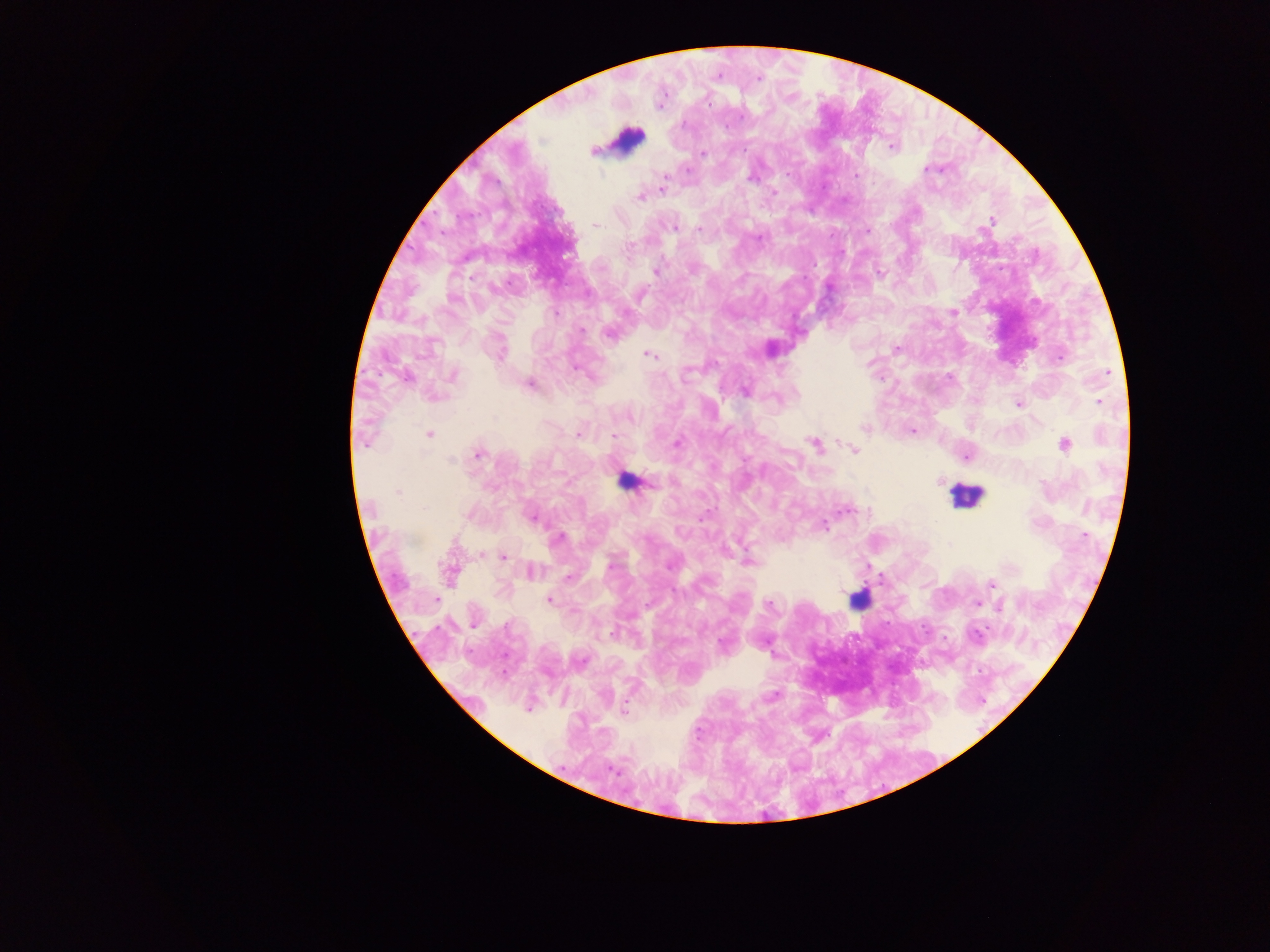
{
  "image_size": "1270×952 pixels",
  "capture": "mobile-phone photograph through a microscope",
  "leukocyte_locations": "approximate centers as {x, y} in pixels: {626, 139}, {626, 482}, {965, 495}, {858, 599}",
  "preparation": "thick blood film",
  "country": "Ghana",
  "malaria_parasite_locations": "approximate centers as {x, y} in pixels: {717, 77}, {759, 78}, {709, 104}, {742, 116}, {891, 147}, {593, 152}, {703, 154}, {687, 169}, {927, 169}, {855, 175}, {664, 178}, {750, 178}, {663, 189}, {774, 192}, {640, 198}, {990, 221}, {595, 224}, {675, 228}, {699, 229}, {867, 231}, {759, 238}, {629, 246}, {655, 271}, {953, 312}, {556, 314}, {582, 330}, {608, 334}, {897, 349}, {501, 354}, {648, 355}, {1060, 357}, {576, 369}, {1107, 373}, {453, 375}, {406, 377}, {685, 378}, {530, 384}, {745, 391}, {1099, 402}, {1018, 404}, {630, 419}, {865, 428}, {913, 431}, {429, 435}, {578, 435}, {614, 435}, {677, 443}, {815, 445}, {1065, 445}, {853, 450}, {479, 454}, {966, 456}, {451, 460}, {940, 481}, {398, 492}, {424, 508}, {847, 510}, {468, 514}, {532, 517}, {824, 525}, {1085, 535}, {559, 538}, {949, 543}, {481, 554}, {504, 557}, {749, 561}, {610, 566}, {531, 570}, {449, 573}, {569, 577}, {991, 584}, {550, 600}, {977, 603}, {769, 605}, {999, 606}, {475, 623}, {613, 633}, {975, 635}, {773, 697}, {625, 709}, {612, 769}",
  "field_of_view": "single"
}